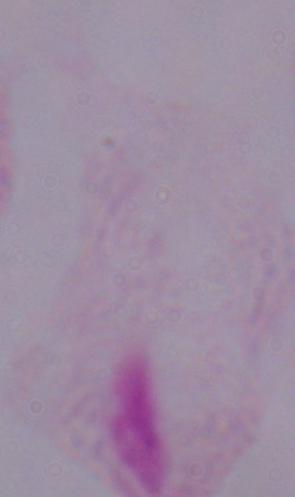

magnification = 1000x
modality = micrograph
identification = trichomonad